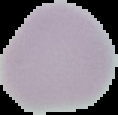

From a thin blood film. Image is 118×115 pixels. Result: negative for malaria parasites. Cell region segmented out of the field of view; the surrounding area is masked to black.